Classify this cell by malaria status.
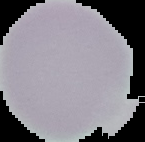

It is uninfected.

Summary:
  - Image size: 145×142 pixels
  - Image type: segmented cell region on a black background
  - Preparation: thin blood smear